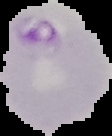 Result: Plasmodium parasites detected. Image is 112×136 pixels. Cell region segmented out of the field of view; the surrounding area is masked to black. From a thin blood smear.